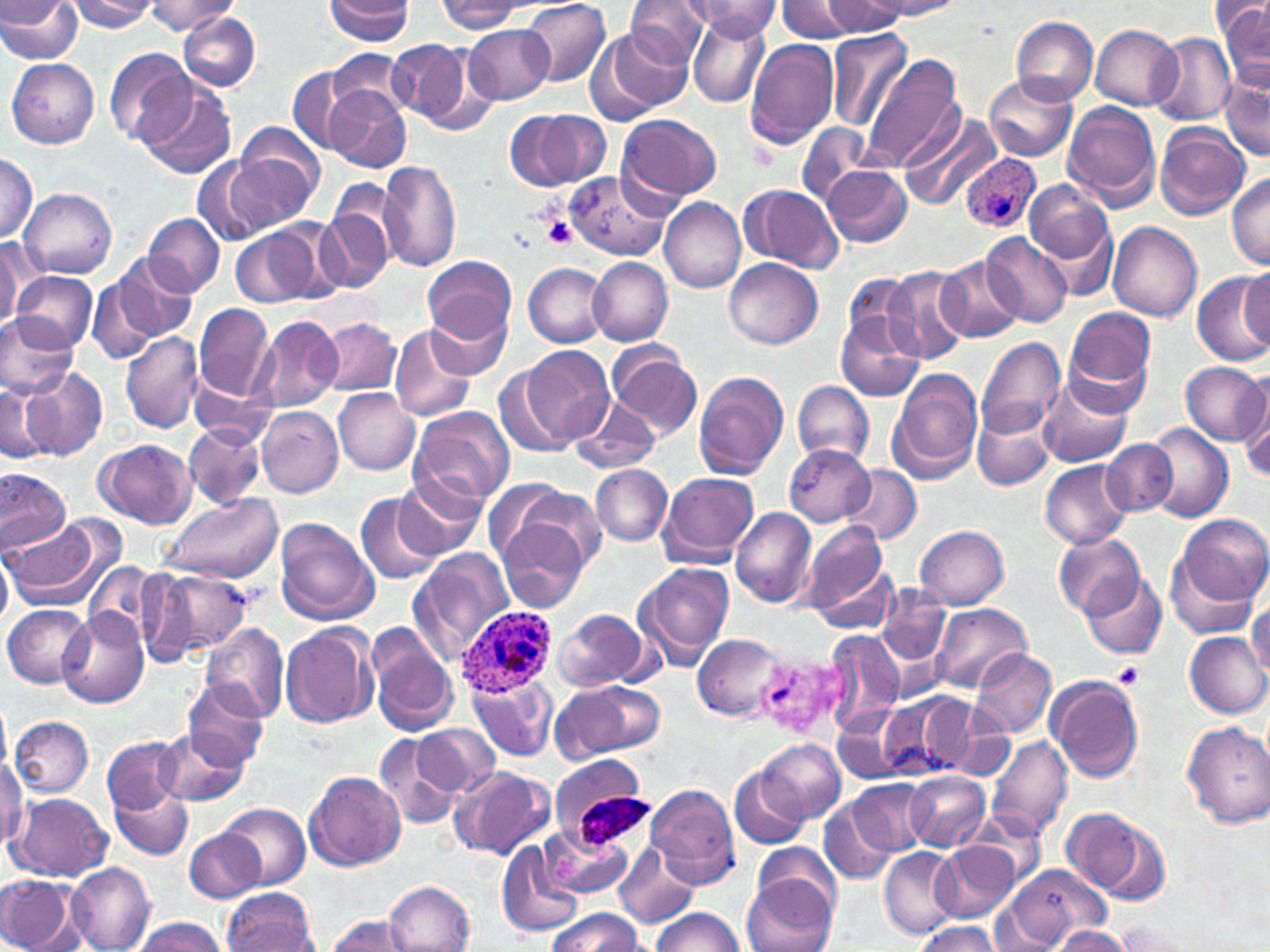 Approximate bounding boxes as (x1,y1)-(x2,y2) corner pairs in pixels. Uninfected red blood cell locations: (0,0)-(83,63), (65,0)-(158,32), (325,0)-(413,44), (520,0)-(611,89), (624,0)-(711,67), (777,0)-(863,42), (438,1)-(520,34), (820,1)-(910,34), (874,1)-(965,20), (1218,1)-(1270,90), (146,2)-(239,34), (687,2)-(783,38), (177,10)-(260,92), (686,11)-(771,107), (1010,15)-(1098,105), (464,25)-(553,103), (1091,26)-(1183,109), (586,28)-(687,122), (825,29)-(914,130), (1149,32)-(1235,125), (387,38)-(488,133), (745,39)-(839,152), (105,48)-(194,147), (329,48)-(414,121), (860,56)-(966,171), (8,59)-(99,148), (288,66)-(363,153), (983,71)-(1076,161), (1220,71)-(1269,164), (136,75)-(237,179), (326,86)-(410,172), (1063,101)-(1161,209), (538,109)-(613,186), (506,112)-(584,190), (616,114)-(723,204), (899,115)-(997,213), (795,124)-(882,206), (1155,124)-(1249,219), (232,130)-(324,230), (1,151)-(37,244), (191,155)-(272,248), (378,160)-(462,274), (821,165)-(912,247), (567,171)-(669,260), (1228,172)-(1270,269), (1025,180)-(1114,265), (739,185)-(843,270), (319,188)-(399,293), (21,189)-(117,277), (659,198)-(747,293), (143,214)-(224,297), (1039,214)-(1119,303), (269,220)-(345,303), (1108,221)-(1201,321), (232,226)-(316,309), (979,233)-(1074,326), (1,237)-(40,329), (111,253)-(195,343), (424,255)-(517,342), (934,255)-(1025,342), (588,257)-(672,345), (725,258)-(822,349), (525,264)-(608,347), (1240,265)-(1269,352), (883,267)-(972,364), (12,272)-(97,351), (844,272)-(924,358), (1192,272)-(1270,366), (88,277)-(159,364), (425,291)-(514,373), (194,304)-(275,405), (163,306)-(273,463), (835,308)-(925,403), (1063,308)-(1157,413), (0,311)-(78,398), (259,315)-(342,412), (318,318)-(400,396), (389,324)-(477,422), (121,331)-(204,435), (975,334)-(1066,442), (607,344)-(703,438), (520,345)-(613,450), (1180,361)-(1269,446), (24,368)-(110,460), (887,371)-(982,483), (692,372)-(789,482), (1040,374)-(1133,468), (188,378)-(275,446), (791,380)-(875,465), (1,381)-(50,462), (1239,384)-(1270,486), (334,389)-(419,475), (567,394)-(662,473), (255,405)-(343,498), (973,406)-(1053,492), (409,407)-(513,507), (183,423)-(265,508), (1145,424)-(1231,524), (94,438)-(196,528), (1101,441)-(1178,516), (784,444)-(875,526), (1040,458)-(1132,549), (592,464)-(672,545), (840,465)-(921,544), (0,469)-(70,556), (394,471)-(484,560), (657,471)-(761,567), (482,476)-(574,568), (520,487)-(605,569), (357,492)-(443,585), (161,495)-(281,583), (730,507)-(816,606), (1172,514)-(1268,608), (5,518)-(104,606), (498,518)-(589,613), (274,519)-(378,625), (802,521)-(889,623), (914,525)-(1009,608), (1053,531)-(1146,620), (411,548)-(514,665), (1166,548)-(1264,642), (0,551)-(12,631), (633,563)-(734,668), (87,565)-(161,643), (139,567)-(253,663), (1080,568)-(1167,659), (877,584)-(948,666), (1248,601)-(1270,678), (932,602)-(1031,692), (4,605)-(94,687), (556,608)-(651,690), (58,611)-(148,708), (281,622)-(377,729), (203,624)-(288,723), (824,627)-(905,730), (1186,631)-(1269,718), (693,632)-(784,721), (368,633)-(460,736), (970,649)-(1057,738), (467,673)-(558,763), (1047,675)-(1143,781), (184,680)-(270,764), (590,683)-(662,752), (550,686)-(630,762), (902,693)-(981,779), (878,698)-(949,777), (0,701)-(11,780), (834,704)-(918,784), (948,715)-(1013,784), (10,716)-(94,798), (1182,720)-(1270,829), (414,724)-(498,796), (156,726)-(249,805), (377,734)-(463,832), (985,735)-(1072,840), (102,736)-(185,813), (762,737)-(845,822), (549,755)-(638,809), (0,756)-(27,845), (451,765)-(553,861), (729,766)-(809,848), (305,770)-(406,871), (905,771)-(990,852), (851,780)-(933,856), (646,784)-(740,887), (112,785)-(193,860), (7,792)-(111,879), (819,800)-(898,886), (222,802)-(309,889), (1062,807)-(1168,904), (964,812)-(1046,888), (540,826)-(633,898), (185,829)-(266,902), (497,842)-(580,939), (614,842)-(700,929), (751,844)-(842,920), (934,844)-(1018,923), (878,847)-(962,940), (67,864)-(155,952), (1003,865)-(1107,947), (0,875)-(81,952), (743,878)-(836,952), (384,880)-(476,951), (222,888)-(317,952), (651,907)-(747,952), (550,909)-(643,952), (324,914)-(419,952), (135,918)-(229,951), (914,921)-(1002,952), (1110,921)-(1203,951), (1046,927)-(1131,952). Platelet locations: (544,216)-(578,249), (1114,664)-(1145,690). Plasmodium ovale-infected red blood cell locations: (961,154)-(1040,232), (457,606)-(554,698). Slide-level diagnosis: Plasmodium ovale. Optical microscopy. Thin blood film. Image is 1270×952 pixels. Single field of view. Captured at 1000x magnification. May-Grünwald-Giemsa stain.